Name the parasite shown.
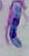
Toxoplasma gondii.

Photomicrograph. 1000x magnification.